Classify this cell by malaria status.
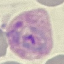
Parasitized.

Summary:
  - Preparation: thin blood film
  - Stain: Giemsa
  - Capture: smartphone camera at the microscope eyepiece
  - Image type: automatically extracted cell patch, resized to 64 × 64 pixels